Name the blood parasite species.
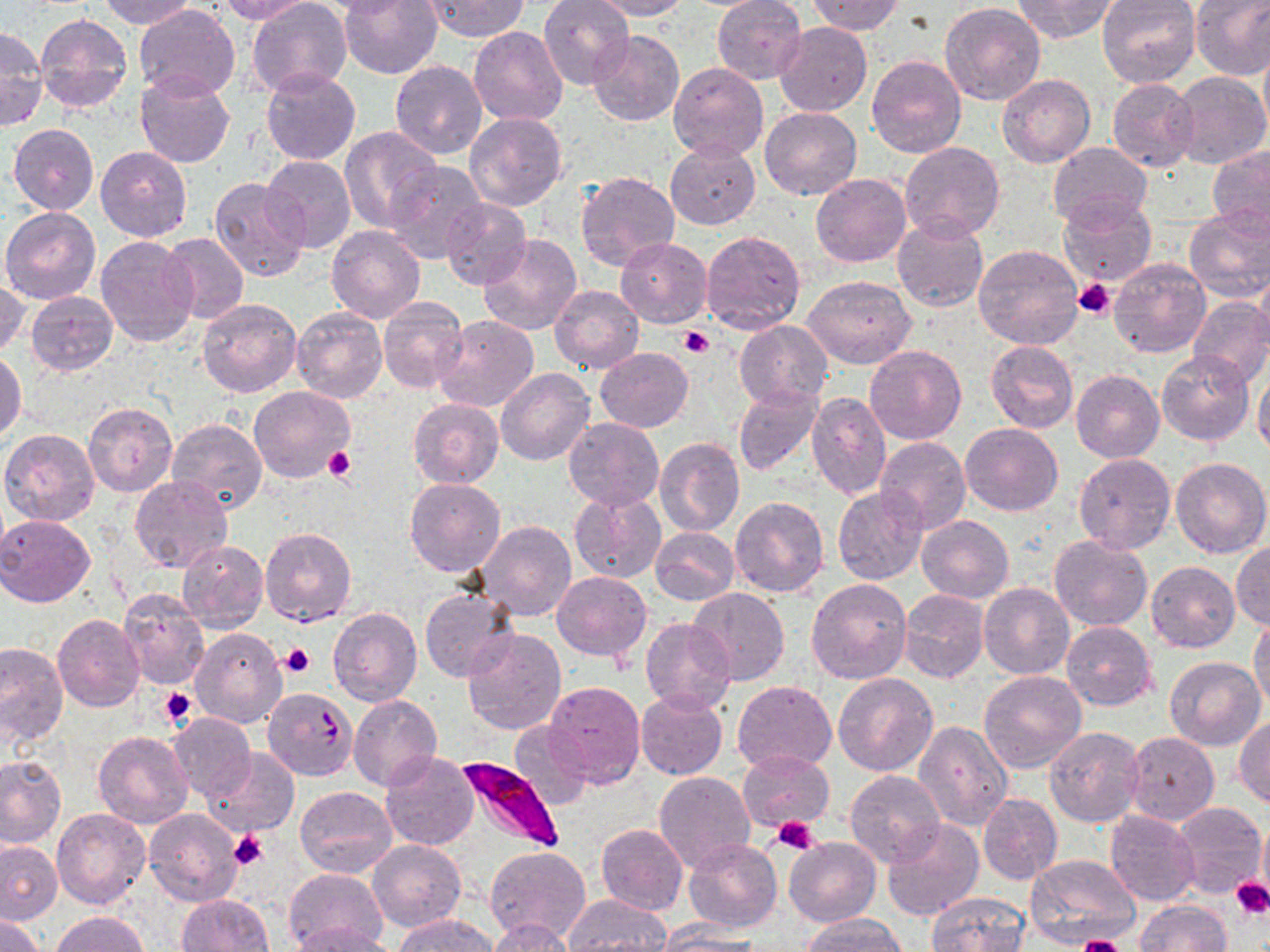
Plasmodium falciparum.

Summary:
  - Coordinate format: approximate bounding boxes as named x1/y1/x2/y2 corners in pixels
  - Platelet locations: (x1=1073, y1=278, x2=1116, y2=319), (x1=678, y1=326, x2=715, y2=358), (x1=323, y1=446, x2=354, y2=483), (x1=281, y1=644, x2=314, y2=678), (x1=160, y1=688, x2=196, y2=730), (x1=772, y1=816, x2=821, y2=854), (x1=230, y1=830, x2=270, y2=869), (x1=1231, y1=877, x2=1270, y2=920), (x1=1074, y1=936, x2=1125, y2=952)
  - Plasmodium falciparum-infected red blood cell locations: (x1=453, y1=758, x2=563, y2=853)
  - Uninfected red blood cell locations: (x1=97, y1=0, x2=199, y2=29), (x1=214, y1=0, x2=313, y2=23), (x1=247, y1=0, x2=353, y2=99), (x1=339, y1=0, x2=442, y2=79), (x1=419, y1=0, x2=528, y2=41), (x1=539, y1=0, x2=635, y2=90), (x1=588, y1=0, x2=692, y2=21), (x1=711, y1=0, x2=806, y2=85), (x1=808, y1=0, x2=905, y2=35), (x1=1010, y1=0, x2=1119, y2=42), (x1=1097, y1=0, x2=1201, y2=88), (x1=1191, y1=0, x2=1270, y2=79), (x1=940, y1=2, x2=1045, y2=105), (x1=135, y1=4, x2=239, y2=101), (x1=36, y1=15, x2=132, y2=112), (x1=774, y1=22, x2=871, y2=116), (x1=0, y1=26, x2=47, y2=131), (x1=469, y1=26, x2=567, y2=125), (x1=589, y1=30, x2=684, y2=126), (x1=1259, y1=47, x2=1270, y2=137), (x1=867, y1=54, x2=966, y2=157), (x1=390, y1=58, x2=487, y2=159), (x1=669, y1=63, x2=768, y2=161), (x1=261, y1=68, x2=360, y2=165), (x1=136, y1=72, x2=234, y2=169), (x1=1168, y1=72, x2=1270, y2=171), (x1=997, y1=75, x2=1095, y2=167), (x1=1106, y1=79, x2=1197, y2=172), (x1=760, y1=106, x2=863, y2=201), (x1=465, y1=113, x2=567, y2=213), (x1=9, y1=124, x2=98, y2=214), (x1=338, y1=126, x2=441, y2=232), (x1=665, y1=141, x2=761, y2=230), (x1=900, y1=142, x2=1005, y2=241), (x1=1048, y1=142, x2=1152, y2=229), (x1=96, y1=146, x2=192, y2=241), (x1=1208, y1=146, x2=1270, y2=237), (x1=261, y1=154, x2=356, y2=253), (x1=384, y1=162, x2=485, y2=265), (x1=576, y1=170, x2=680, y2=270), (x1=811, y1=173, x2=910, y2=266), (x1=210, y1=177, x2=311, y2=282), (x1=1058, y1=196, x2=1156, y2=288), (x1=440, y1=202, x2=530, y2=287), (x1=1184, y1=206, x2=1270, y2=304), (x1=1, y1=207, x2=100, y2=304), (x1=892, y1=217, x2=990, y2=313), (x1=327, y1=226, x2=426, y2=324), (x1=701, y1=228, x2=805, y2=334), (x1=158, y1=231, x2=249, y2=325), (x1=478, y1=234, x2=582, y2=337), (x1=96, y1=235, x2=200, y2=348), (x1=614, y1=237, x2=712, y2=327), (x1=973, y1=244, x2=1084, y2=350), (x1=1108, y1=257, x2=1212, y2=358), (x1=1256, y1=263, x2=1270, y2=347), (x1=803, y1=273, x2=917, y2=368), (x1=0, y1=281, x2=29, y2=357), (x1=551, y1=285, x2=644, y2=374), (x1=26, y1=290, x2=118, y2=376), (x1=378, y1=297, x2=468, y2=392), (x1=1187, y1=297, x2=1270, y2=388), (x1=197, y1=298, x2=301, y2=397), (x1=292, y1=306, x2=387, y2=403), (x1=432, y1=315, x2=539, y2=411), (x1=735, y1=321, x2=832, y2=411), (x1=987, y1=340, x2=1078, y2=432), (x1=865, y1=344, x2=966, y2=444), (x1=594, y1=347, x2=693, y2=431), (x1=0, y1=350, x2=24, y2=443), (x1=1158, y1=351, x2=1253, y2=445), (x1=496, y1=369, x2=594, y2=467), (x1=1253, y1=369, x2=1270, y2=458), (x1=1072, y1=370, x2=1164, y2=464), (x1=249, y1=386, x2=355, y2=483), (x1=734, y1=386, x2=822, y2=475), (x1=806, y1=392, x2=891, y2=500), (x1=409, y1=398, x2=503, y2=486), (x1=84, y1=401, x2=177, y2=496), (x1=167, y1=417, x2=267, y2=515), (x1=564, y1=418, x2=664, y2=511), (x1=960, y1=423, x2=1062, y2=516), (x1=1, y1=429, x2=99, y2=525), (x1=875, y1=437, x2=971, y2=536), (x1=656, y1=438, x2=744, y2=536), (x1=1074, y1=453, x2=1175, y2=555), (x1=1170, y1=457, x2=1270, y2=557), (x1=130, y1=476, x2=233, y2=573), (x1=404, y1=479, x2=506, y2=576), (x1=833, y1=486, x2=929, y2=585), (x1=570, y1=491, x2=666, y2=584), (x1=730, y1=496, x2=830, y2=597), (x1=0, y1=514, x2=98, y2=607), (x1=915, y1=514, x2=1013, y2=604), (x1=473, y1=521, x2=576, y2=621), (x1=260, y1=527, x2=357, y2=626), (x1=649, y1=527, x2=739, y2=605), (x1=1049, y1=536, x2=1153, y2=630), (x1=177, y1=540, x2=268, y2=631), (x1=1231, y1=541, x2=1270, y2=630), (x1=1146, y1=562, x2=1240, y2=653), (x1=551, y1=571, x2=650, y2=660), (x1=806, y1=577, x2=913, y2=684), (x1=979, y1=582, x2=1074, y2=679), (x1=688, y1=588, x2=790, y2=686), (x1=421, y1=589, x2=518, y2=682), (x1=898, y1=590, x2=989, y2=684), (x1=118, y1=591, x2=210, y2=690), (x1=138, y1=602, x2=252, y2=711), (x1=329, y1=606, x2=422, y2=706), (x1=53, y1=614, x2=145, y2=712), (x1=1249, y1=615, x2=1270, y2=712), (x1=640, y1=618, x2=736, y2=715), (x1=1061, y1=622, x2=1156, y2=710), (x1=191, y1=627, x2=286, y2=728), (x1=463, y1=627, x2=566, y2=734), (x1=0, y1=642, x2=68, y2=747), (x1=1164, y1=656, x2=1265, y2=750), (x1=978, y1=670, x2=1088, y2=773), (x1=833, y1=672, x2=938, y2=777), (x1=733, y1=679, x2=837, y2=772), (x1=545, y1=682, x2=645, y2=786), (x1=262, y1=688, x2=358, y2=780), (x1=634, y1=690, x2=728, y2=779), (x1=348, y1=695, x2=440, y2=791), (x1=168, y1=713, x2=256, y2=801), (x1=1234, y1=716, x2=1270, y2=807), (x1=913, y1=720, x2=1012, y2=831), (x1=509, y1=721, x2=593, y2=810), (x1=1044, y1=726, x2=1145, y2=827), (x1=93, y1=730, x2=194, y2=829), (x1=1124, y1=732, x2=1219, y2=825), (x1=202, y1=747, x2=300, y2=838), (x1=736, y1=750, x2=835, y2=833), (x1=380, y1=752, x2=479, y2=851), (x1=0, y1=755, x2=66, y2=848), (x1=845, y1=768, x2=943, y2=866), (x1=654, y1=769, x2=755, y2=873), (x1=294, y1=785, x2=396, y2=878), (x1=977, y1=793, x2=1062, y2=884), (x1=1169, y1=802, x2=1268, y2=901), (x1=144, y1=808, x2=243, y2=906), (x1=52, y1=810, x2=151, y2=910), (x1=1104, y1=811, x2=1201, y2=907), (x1=880, y1=819, x2=984, y2=920), (x1=595, y1=823, x2=688, y2=915), (x1=785, y1=837, x2=880, y2=927), (x1=0, y1=839, x2=63, y2=925), (x1=370, y1=839, x2=465, y2=932), (x1=685, y1=839, x2=782, y2=932), (x1=485, y1=846, x2=589, y2=944), (x1=1025, y1=853, x2=1141, y2=949), (x1=283, y1=867, x2=390, y2=951), (x1=925, y1=891, x2=1031, y2=952), (x1=177, y1=894, x2=275, y2=951), (x1=563, y1=894, x2=670, y2=952), (x1=1136, y1=900, x2=1230, y2=951), (x1=0, y1=912, x2=45, y2=951), (x1=52, y1=912, x2=149, y2=951), (x1=800, y1=912, x2=907, y2=951), (x1=394, y1=914, x2=500, y2=952), (x1=486, y1=918, x2=579, y2=952), (x1=653, y1=921, x2=765, y2=951), (x1=291, y1=923, x2=395, y2=952)
  - Field of view: single
  - Modality: optical microscopy
  - Stain: May-Grünwald-Giemsa
  - Image size: 1270×952 pixels
  - Magnification: 1000x
  - Preparation: thin blood smear